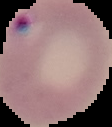

Summary:
  - Malaria status: parasitized
  - Image type: segmented cell region with the area outside set to black
  - Preparation: thin blood smear
  - Image size: 112×127 pixels